Classify this cell by malaria status.
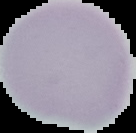

Uninfected.

Summary:
  - Image size: 136×133 pixels
  - Image type: segmented cell region with the area outside set to black
  - Preparation: thin blood film